Locate and identify every blood parasite.
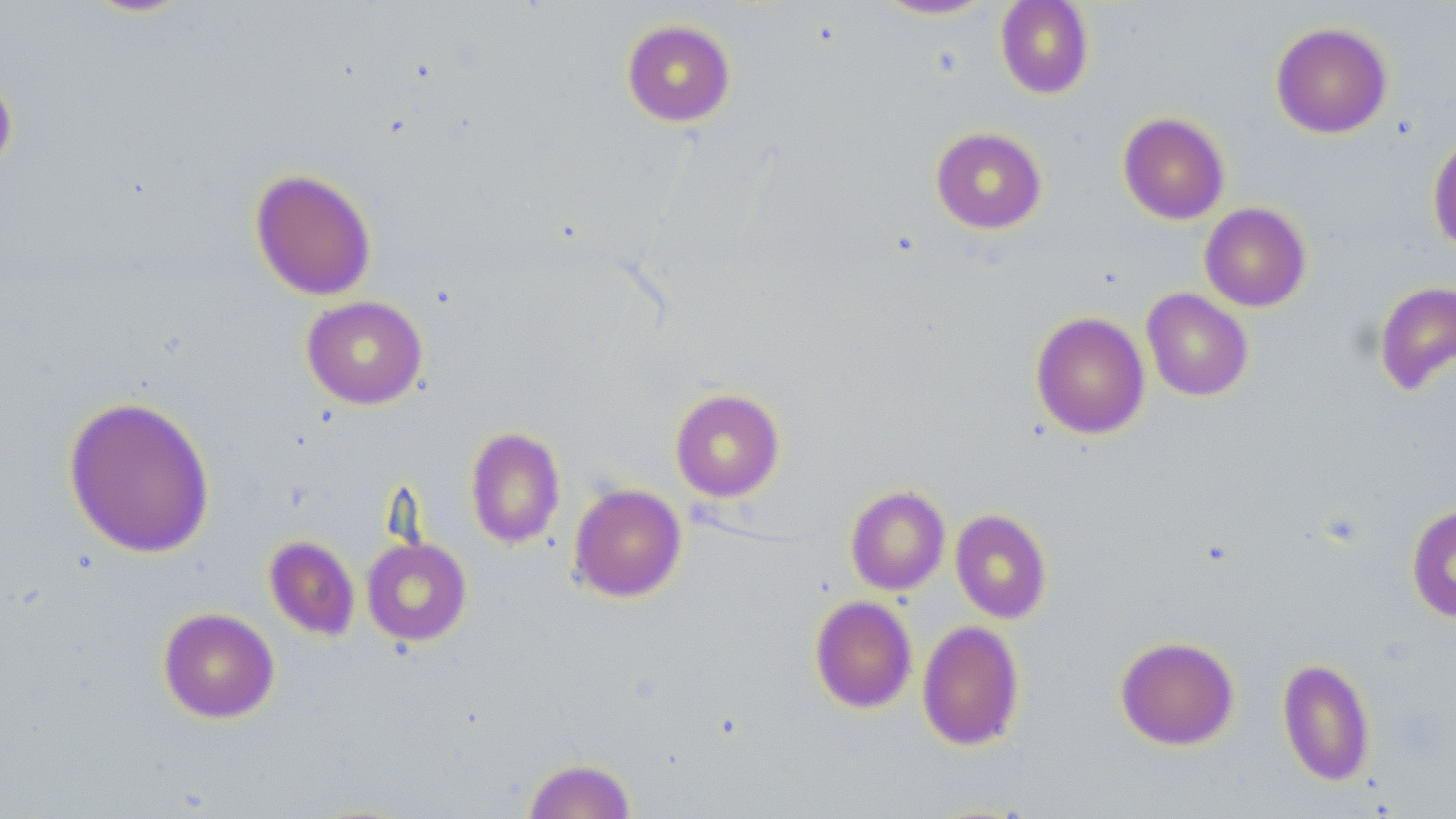
No blood parasites seen.

Summary:
  - Coordinate format: approximate bounding boxes as named x1/y1/x2/y2 corners in pixels
  - Uninfected red blood cell locations: (x1=873, y1=0, x2=997, y2=20), (x1=995, y1=0, x2=1095, y2=99), (x1=621, y1=19, x2=736, y2=127), (x1=1270, y1=21, x2=1393, y2=139), (x1=0, y1=67, x2=18, y2=180), (x1=1117, y1=112, x2=1230, y2=225), (x1=930, y1=127, x2=1047, y2=234), (x1=1428, y1=132, x2=1456, y2=257), (x1=249, y1=168, x2=377, y2=301), (x1=1199, y1=202, x2=1312, y2=312), (x1=1373, y1=281, x2=1456, y2=397), (x1=1141, y1=288, x2=1254, y2=401), (x1=302, y1=295, x2=428, y2=409), (x1=1030, y1=311, x2=1150, y2=440), (x1=669, y1=388, x2=785, y2=501), (x1=63, y1=395, x2=216, y2=559), (x1=465, y1=427, x2=566, y2=549), (x1=568, y1=484, x2=687, y2=603), (x1=845, y1=485, x2=950, y2=595), (x1=1406, y1=503, x2=1456, y2=624), (x1=950, y1=509, x2=1052, y2=624), (x1=264, y1=535, x2=360, y2=640), (x1=361, y1=537, x2=472, y2=646), (x1=809, y1=595, x2=917, y2=713), (x1=158, y1=607, x2=280, y2=723), (x1=917, y1=620, x2=1025, y2=751), (x1=1115, y1=635, x2=1240, y2=751), (x1=1277, y1=657, x2=1376, y2=786), (x1=522, y1=758, x2=636, y2=819)
  - Slide-level diagnosis: no evidence of blood parasites
  - Field of view: single
  - Image size: 1456×819 pixels
  - Magnification: 1000x
  - Preparation: thin blood film
  - Modality: optical microscopy
  - Stain: May-Grünwald-Giemsa